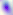

{
  "magnification": "400x",
  "identification": "Toxoplasma gondii",
  "modality": "micrograph"
}